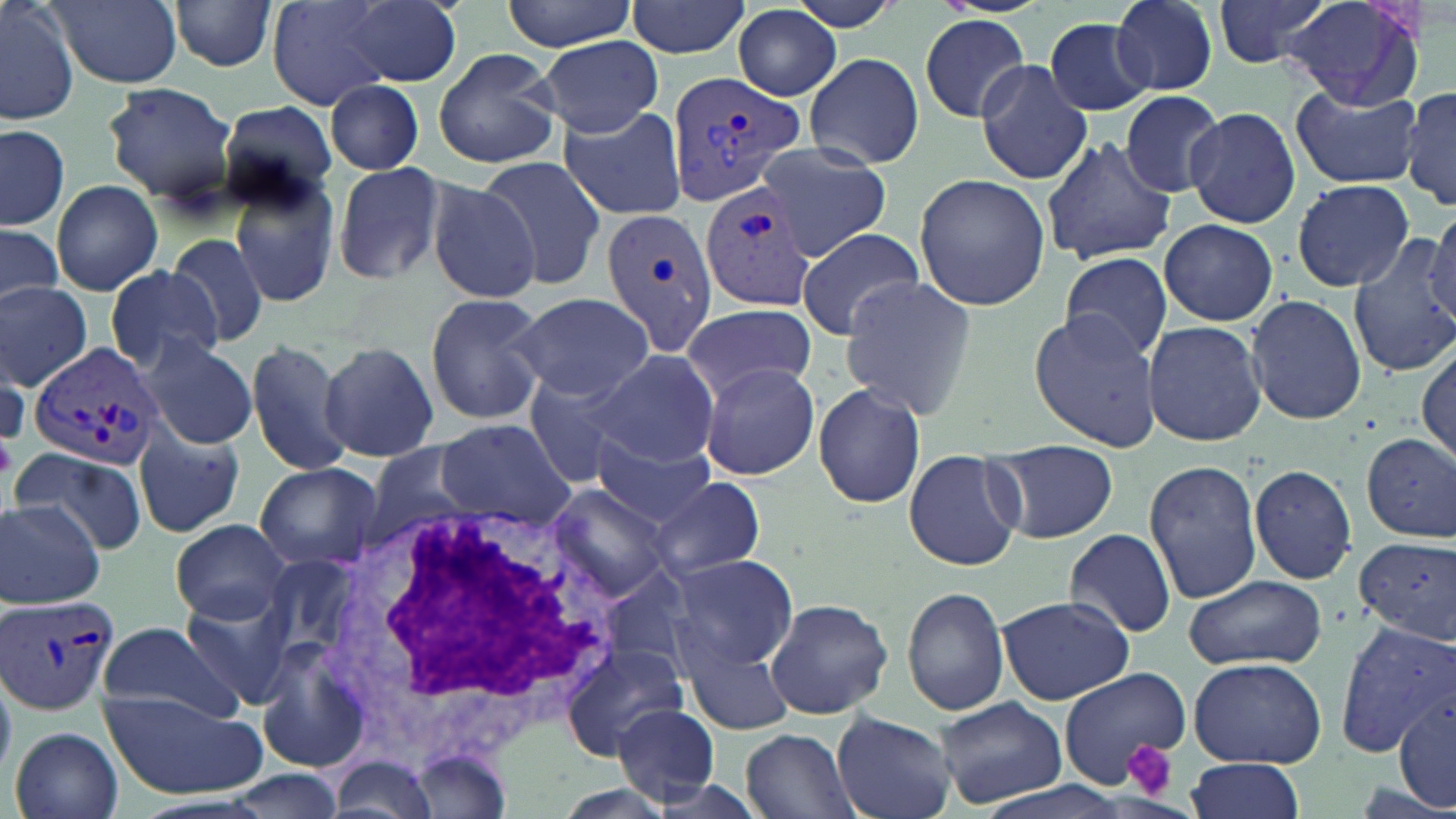 Approximate bounding boxes as [x1, y1, x2, y2] in pixels. White blood cell locations: [299, 490, 638, 770]. Uninfected red blood cell locations: [0, 0, 77, 126], [45, 0, 183, 88], [168, 0, 280, 73], [349, 0, 462, 86], [503, 0, 636, 51], [626, 0, 753, 60], [785, 0, 910, 33], [1108, 0, 1218, 96], [1212, 0, 1329, 69], [1277, 0, 1428, 111], [265, 1, 397, 111], [733, 6, 843, 102], [919, 15, 1029, 123], [1046, 17, 1158, 118], [538, 37, 664, 136], [433, 47, 562, 169], [805, 53, 926, 169], [974, 60, 1093, 185], [323, 77, 426, 176], [101, 82, 239, 206], [1291, 83, 1426, 190], [1401, 86, 1456, 210], [1121, 90, 1229, 197], [219, 101, 337, 207], [557, 103, 690, 223], [1184, 105, 1303, 228], [0, 123, 70, 231], [1041, 136, 1175, 265], [755, 142, 892, 258], [475, 156, 607, 287], [331, 162, 445, 285], [914, 172, 1051, 310], [229, 176, 340, 310], [1290, 178, 1416, 292], [423, 179, 543, 305], [51, 180, 163, 295], [1426, 210, 1456, 326], [1157, 217, 1279, 326], [0, 224, 64, 311], [797, 226, 924, 340], [164, 232, 271, 350], [1347, 235, 1456, 380], [1061, 252, 1172, 361], [102, 265, 225, 374], [841, 276, 978, 417], [0, 282, 93, 390], [423, 292, 549, 427], [510, 292, 657, 405], [1245, 293, 1366, 426], [683, 303, 815, 404], [1029, 309, 1163, 453], [1143, 320, 1268, 446], [141, 336, 258, 449], [244, 337, 354, 475], [320, 340, 439, 463], [1416, 342, 1455, 465], [0, 348, 29, 447], [592, 348, 722, 469], [697, 361, 821, 480], [521, 371, 645, 487], [813, 382, 925, 508], [435, 419, 573, 526], [134, 425, 246, 539], [591, 432, 717, 527], [1361, 433, 1456, 543], [986, 439, 1119, 545], [368, 444, 482, 539], [11, 445, 147, 555], [903, 448, 1025, 572], [1143, 459, 1265, 603], [253, 463, 380, 569], [1248, 463, 1357, 586], [650, 476, 766, 580], [548, 486, 671, 603], [1, 500, 106, 608], [169, 517, 293, 625], [1064, 528, 1175, 638], [1356, 538, 1456, 641], [665, 552, 799, 673], [597, 567, 692, 674], [1183, 574, 1325, 670], [179, 579, 305, 711], [902, 587, 1011, 716], [997, 595, 1133, 706], [764, 597, 893, 720], [95, 620, 244, 723], [1335, 620, 1455, 758], [681, 629, 800, 737], [255, 636, 373, 771], [560, 643, 689, 760], [1190, 656, 1327, 767], [1056, 668, 1189, 789], [1394, 689, 1454, 814], [101, 692, 265, 802], [937, 699, 1068, 807], [611, 703, 722, 806], [831, 711, 957, 819], [11, 727, 124, 819], [742, 728, 855, 818], [330, 754, 441, 819], [1185, 756, 1306, 818], [221, 767, 340, 818], [642, 777, 770, 818]. Plasmodium vivax-infected red blood cell locations: [667, 71, 808, 212], [698, 178, 819, 313], [600, 207, 722, 358], [26, 341, 162, 472], [0, 595, 120, 717]. Platelet locations: [0, 426, 17, 486], [1125, 738, 1179, 799]. Slide-level diagnosis: Plasmodium vivax. May-Grünwald-Giemsa-stained preparation. Thin blood film. Image is 1456×819 pixels. Light microscopy. Single field of view. Captured at 1000x magnification.